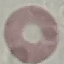
Result: no malaria parasites detected. Giemsa-stained preparation. Thin smear of blood. Automatically extracted cell patch, resized to 64 × 64 pixels. Acquired by smartphone through the microscope eyepiece.